Classify this cell by malaria status.
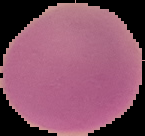

Uninfected.

Segmented cell region on a black background. From a thin blood film. Image is 145×136 pixels.